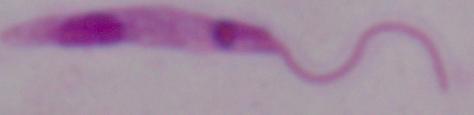
magnification = 1000x
modality = micrograph
identification = Leishmania